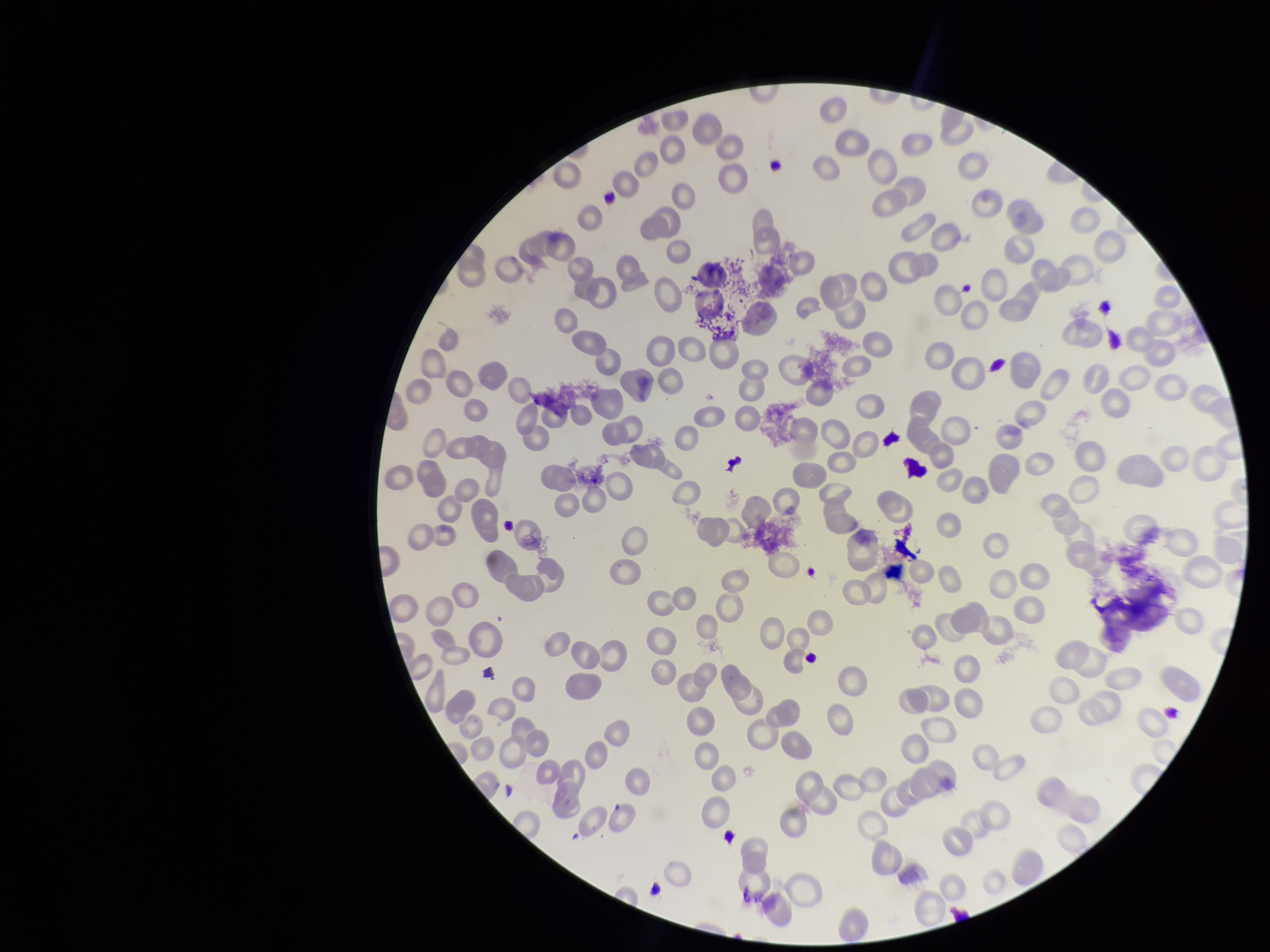

Summary:
  - Red blood cell count: 171
  - Preparation: thin smear
  - Capture: smartphone photograph through the microscope eyepiece
  - Stain: Giemsa
  - Parasitized red blood cells: none seen
  - Image size: 1270×952 pixels
  - Parasitized red blood cell count: 0
  - Patient malaria status: negative
  - Field of view: single